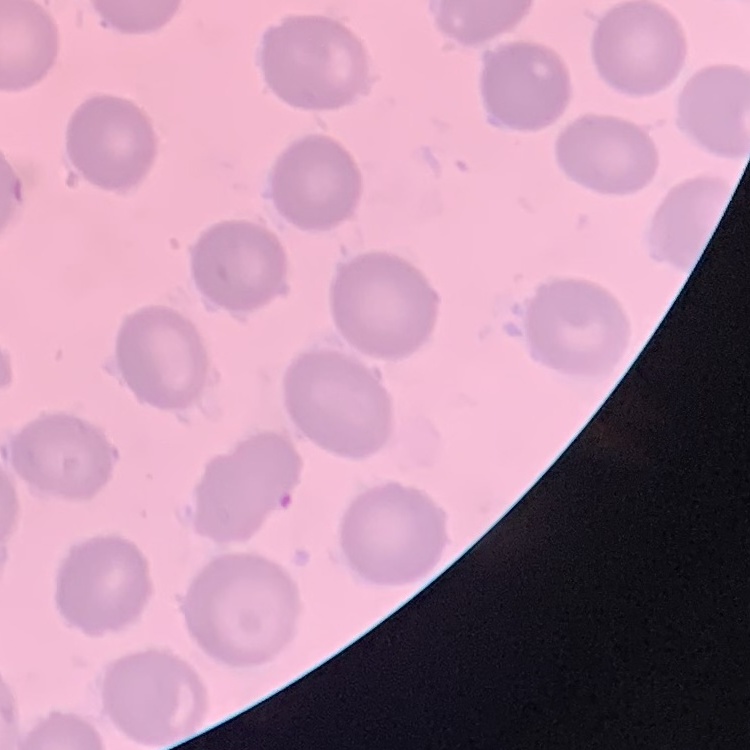
Summary:
  - Red blood cell morphology: no rouleaux formation
  - Stain: Field's or Giemsa
  - Image type: square crop of a larger photomicrograph
  - Preparation: thin blood film